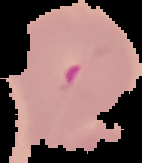

Result: Plasmodium parasites identified. From a thin blood smear. Image is 142×163 pixels. The area outside the segmented cell region is set to black.